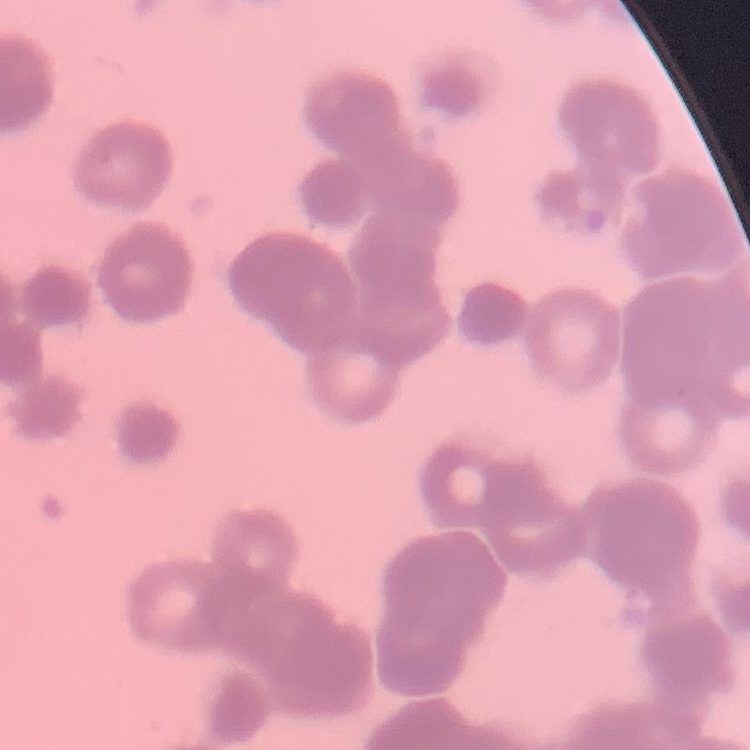

The red blood cells show rouleaux formation. Stained with either Field's or Giemsa. One tile cut from a larger photomicrograph. Thin blood film.